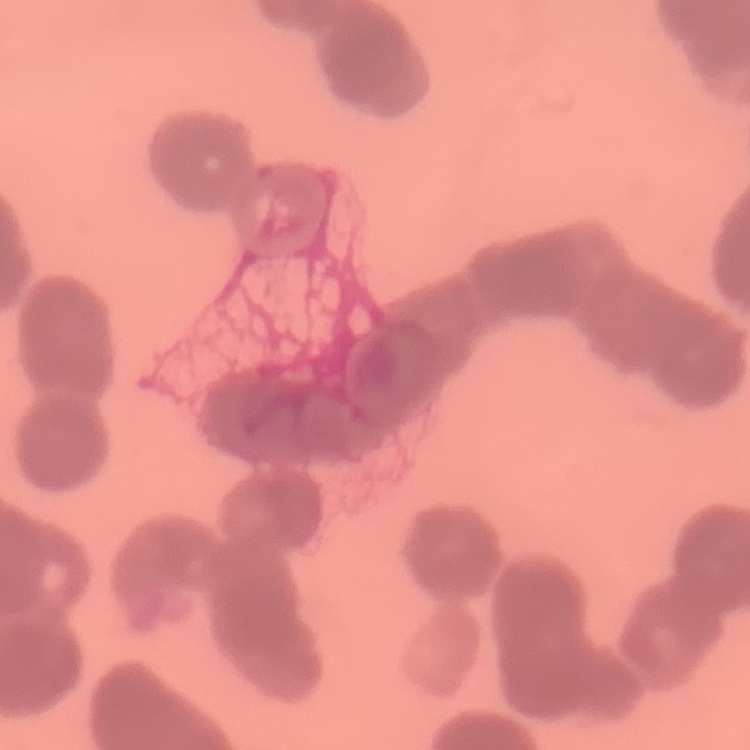

erythrocyte_morphology: rouleaux formation
preparation: thin blood smear
image_type: square crop of a larger photomicrograph
stain: Field's or Giemsa